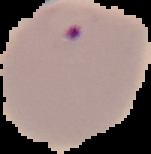

image_type: segmented cell region on a black background
result: malaria parasites detected
image_size: 151×154 pixels
preparation: thin blood smear